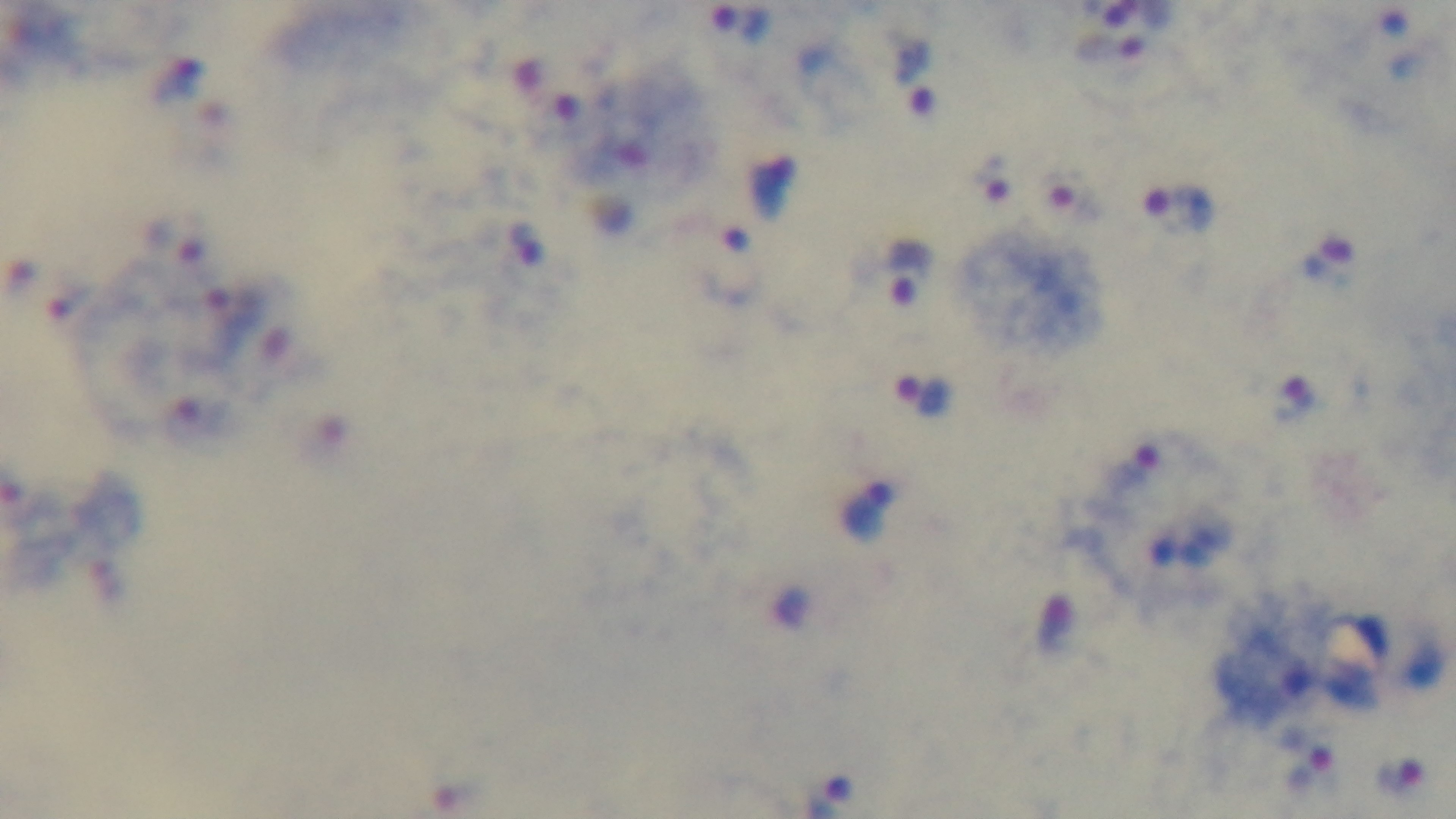
Summary:
  - Capture: mounted 4K digital camera
  - Malaria status: infected
  - Objective: 100x oil immersion
  - Stain: Giemsa
  - Field of view: one from the slide
  - Modality: light microscopy
  - Preparation: thick blood film